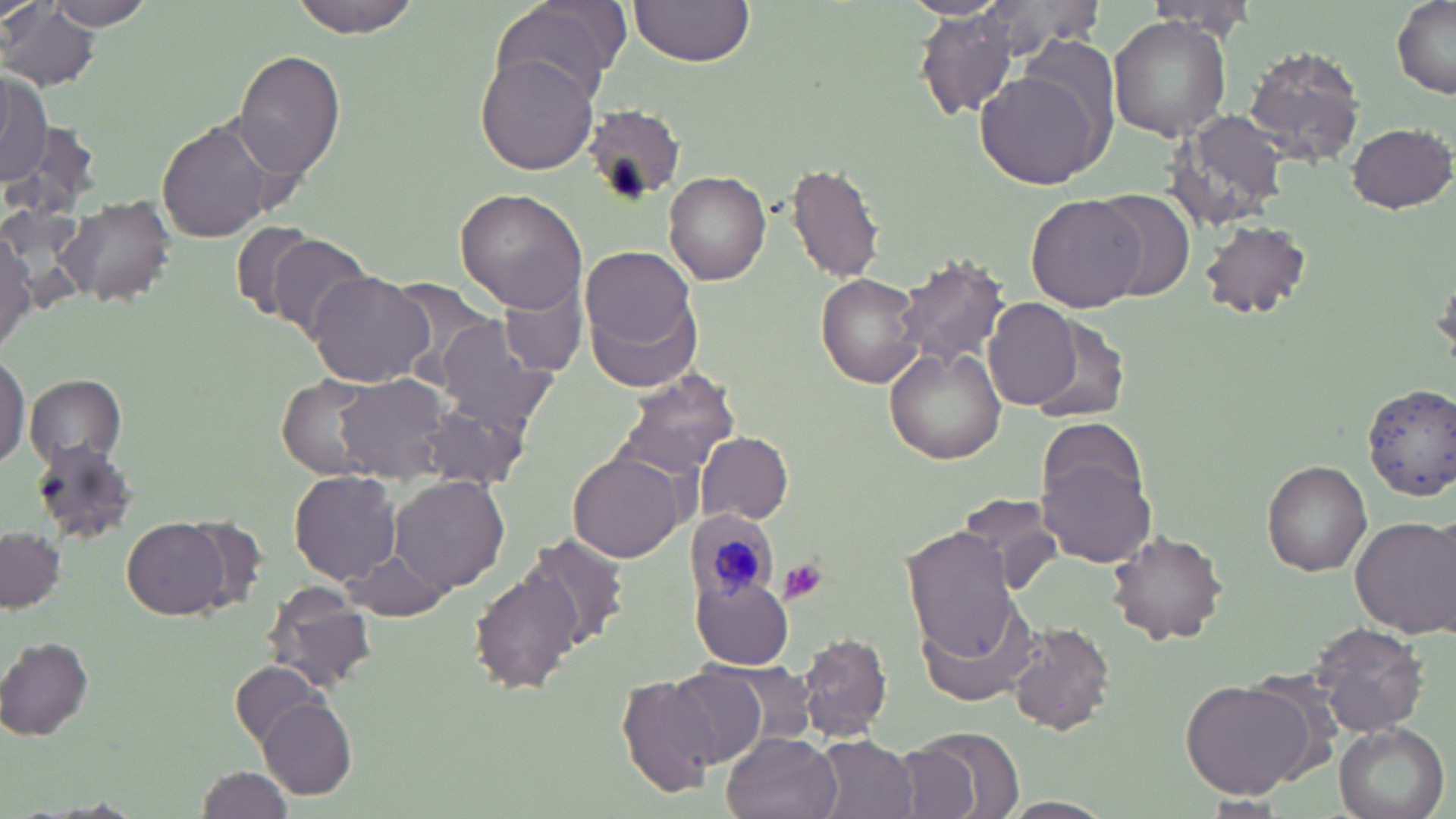 Approximate bounding boxes as (x1,y1)-(x2,y2) corner pairs in pixels. Platelet locations: (780,559)-(828,604). Uninfected red blood cell locations: (289,0)-(422,36), (491,0)-(626,104), (628,0)-(753,68), (969,0)-(1108,58), (1389,0)-(1456,101), (50,1)-(151,29), (1143,3)-(1261,42), (3,4)-(96,90), (916,5)-(1024,121), (1108,16)-(1233,139), (1019,36)-(1119,147), (1243,43)-(1368,168), (233,49)-(346,183), (475,53)-(597,174), (0,70)-(50,189), (977,70)-(1107,186), (581,106)-(685,203), (1168,109)-(1295,228), (157,117)-(287,243), (1346,120)-(1455,213), (786,162)-(884,283), (664,170)-(771,286), (1092,187)-(1196,301), (456,188)-(590,311), (1027,195)-(1143,313), (60,197)-(178,306), (1199,219)-(1314,320), (231,221)-(318,319), (0,231)-(36,351), (264,233)-(370,341), (582,251)-(701,390), (892,254)-(1011,371), (307,271)-(436,387), (816,273)-(924,387), (502,281)-(585,375), (984,297)-(1082,408), (1026,317)-(1129,425), (435,319)-(558,433), (883,348)-(1005,465), (0,353)-(25,469), (613,367)-(739,482), (25,374)-(127,466), (336,374)-(450,484), (279,376)-(383,479), (1361,381)-(1456,501), (416,403)-(531,490), (695,432)-(792,524), (31,440)-(138,545), (1037,449)-(1157,568), (570,452)-(684,563), (1262,460)-(1372,577), (289,470)-(403,585), (391,475)-(508,594), (955,493)-(1060,592), (1350,514)-(1456,638), (123,516)-(230,619), (901,526)-(1023,660), (1,528)-(64,612), (1107,530)-(1230,646), (524,533)-(630,651), (341,545)-(449,621), (474,567)-(583,693), (691,575)-(795,668), (262,583)-(378,692), (912,599)-(1040,710), (1008,621)-(1116,735), (1313,622)-(1431,736), (799,632)-(893,743), (0,637)-(95,741), (695,658)-(820,762), (229,661)-(329,750), (661,665)-(770,768), (616,673)-(724,798), (1181,678)-(1317,800), (257,699)-(357,798), (1333,720)-(1450,819), (905,727)-(1023,818), (723,731)-(841,819), (814,735)-(918,819), (193,766)-(291,817), (1201,795)-(1288,814), (1000,797)-(1114,819). Plasmodium malariae-infected red blood cell locations: (691,514)-(777,605). Slide-level diagnosis: Plasmodium malariae. May-Grünwald-Giemsa stain. Thin blood film. Single field of view. Image is 1456×819 pixels. Light microscopy. 1000x magnification.